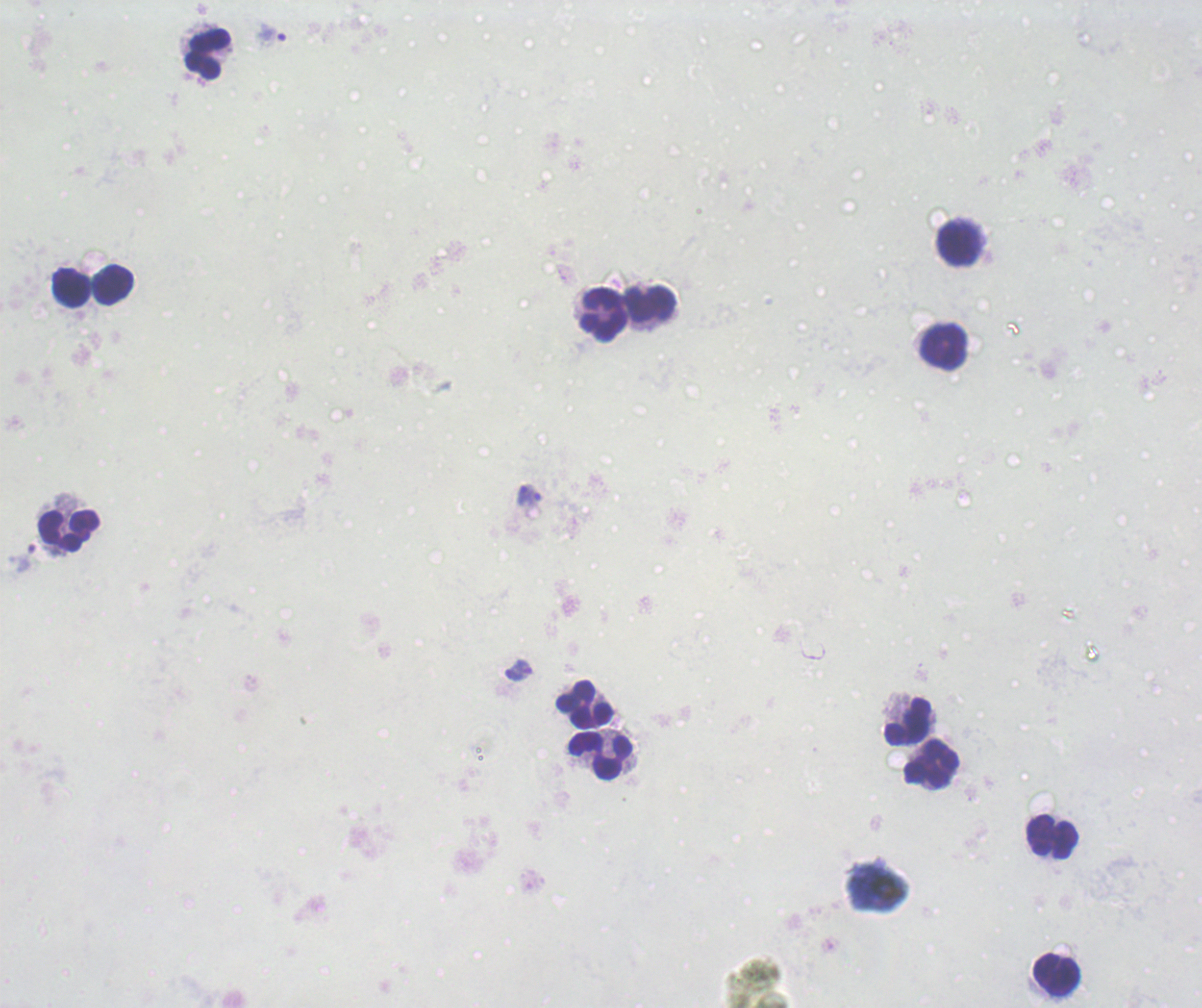
Approximate object centers, in pixels from the top-left corner. Leukocyte locations: (x=207, y=54), (x=959, y=242), (x=113, y=284), (x=70, y=286), (x=651, y=304), (x=603, y=315), (x=944, y=346), (x=69, y=529), (x=585, y=704), (x=907, y=721), (x=600, y=755), (x=931, y=765), (x=1052, y=835), (x=1056, y=975). Trophozoite locations: (x=272, y=35), (x=529, y=495), (x=22, y=557), (x=518, y=670). Romanowsky stain. Result: positive for malaria parasites. Previously used in a real diagnosis. Captured at 100x magnification. Background quality: unsatisfactory. Thick smear of blood. One field from this slide. Image is 1202×1008 pixels.